Assess the morphology of the red blood cells.
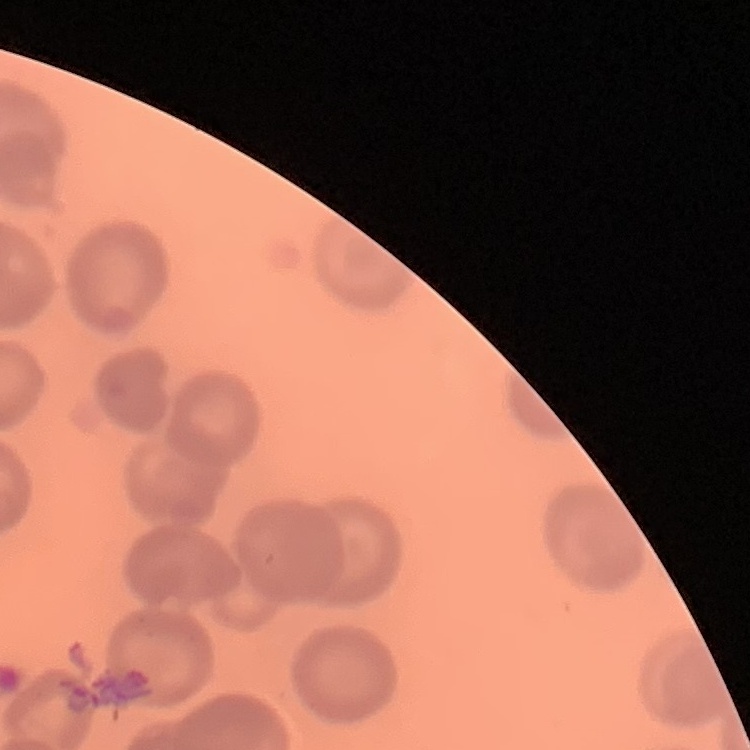
No rouleaux formation.

Summary:
  - Stain: Field's or Giemsa
  - Image type: one tile cut from a larger photomicrograph
  - Preparation: thin peripheral smear